Assess the morphology of the red blood cells.
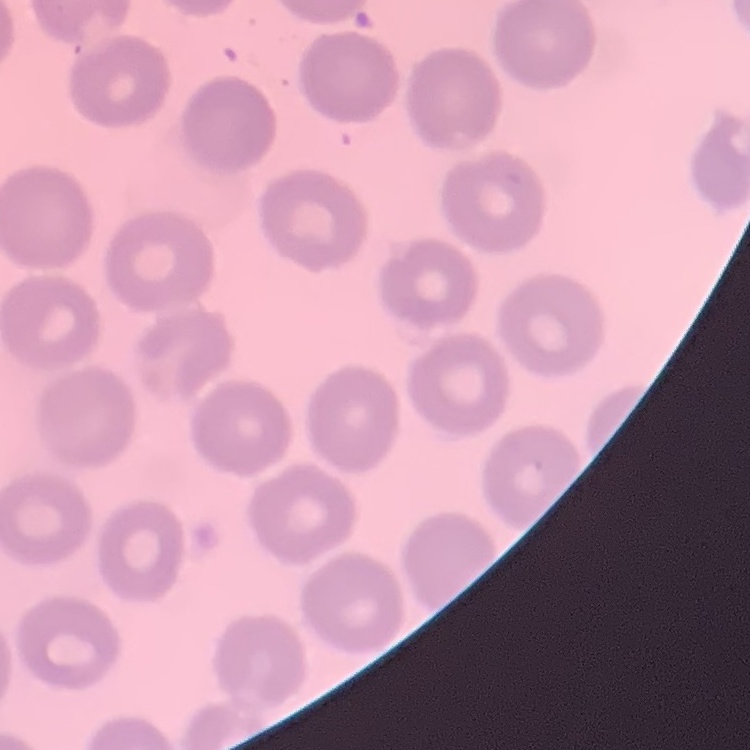

They show no rouleaux formation.

image_type: square crop of a larger photomicrograph
preparation: thin blood smear
stain: Field's or Giemsa